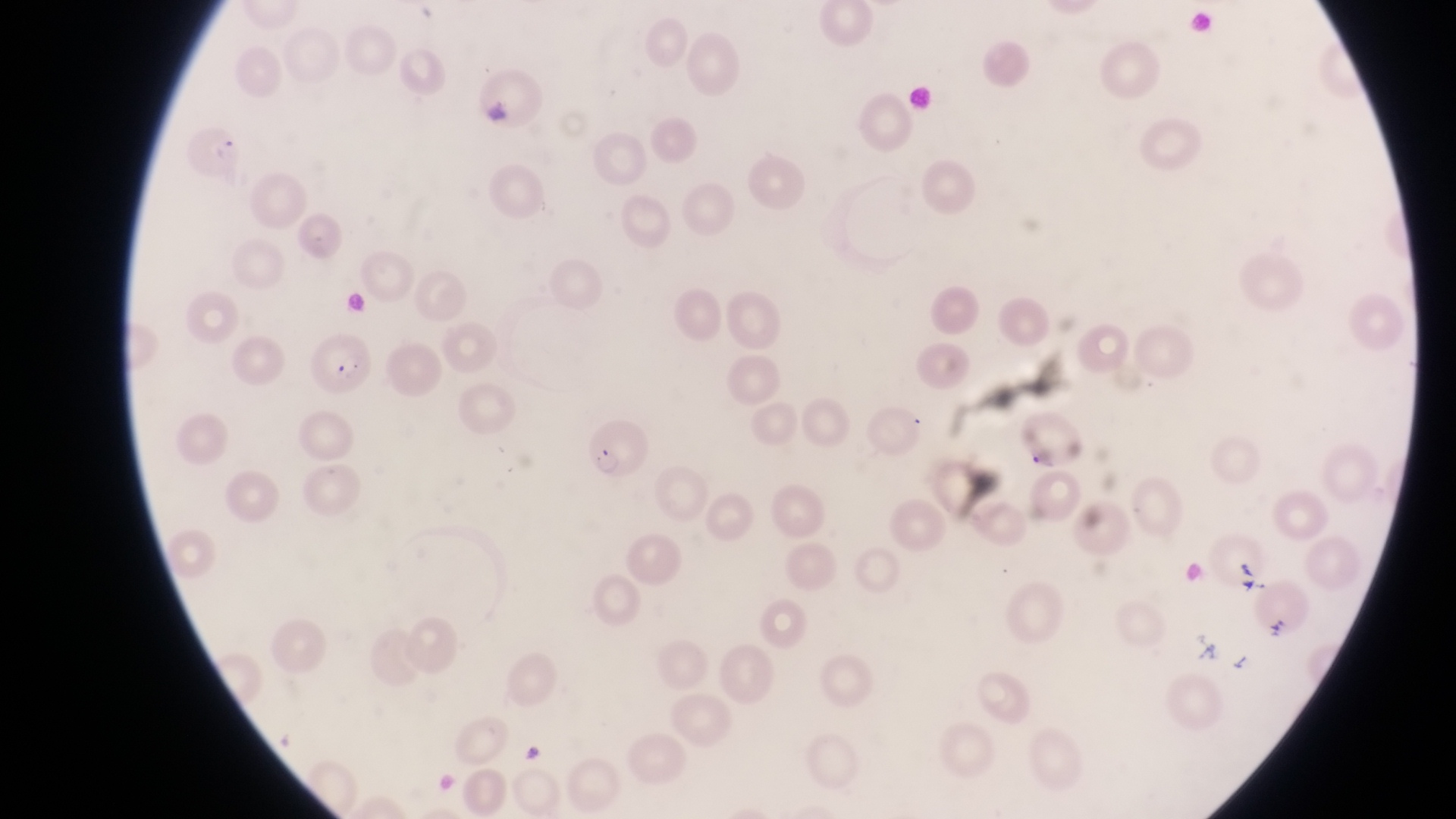

Approximate bounding boxes as left top right bottom in pixels. Parasitised red blood cell locations: 190 121 239 180; 312 337 380 396; 581 417 648 478. Artifact (platelet-like body, stain precipitate, or debris) locations: 1235 557 1262 593; 1266 612 1294 648. Image is 1456×819 pixels. Captured by a smartphone held over the eyepiece of an Olympus CX-23 microscope. Collected in Uganda. Thin blood film. One field of view. Magnification of 1000x.